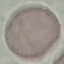

Summary:
  - Result: no malaria parasites detected
  - Image type: automatically extracted cell patch, resized to 64 × 64 pixels
  - Preparation: thin blood film
  - Capture: smartphone camera at the microscope eyepiece
  - Stain: Giemsa